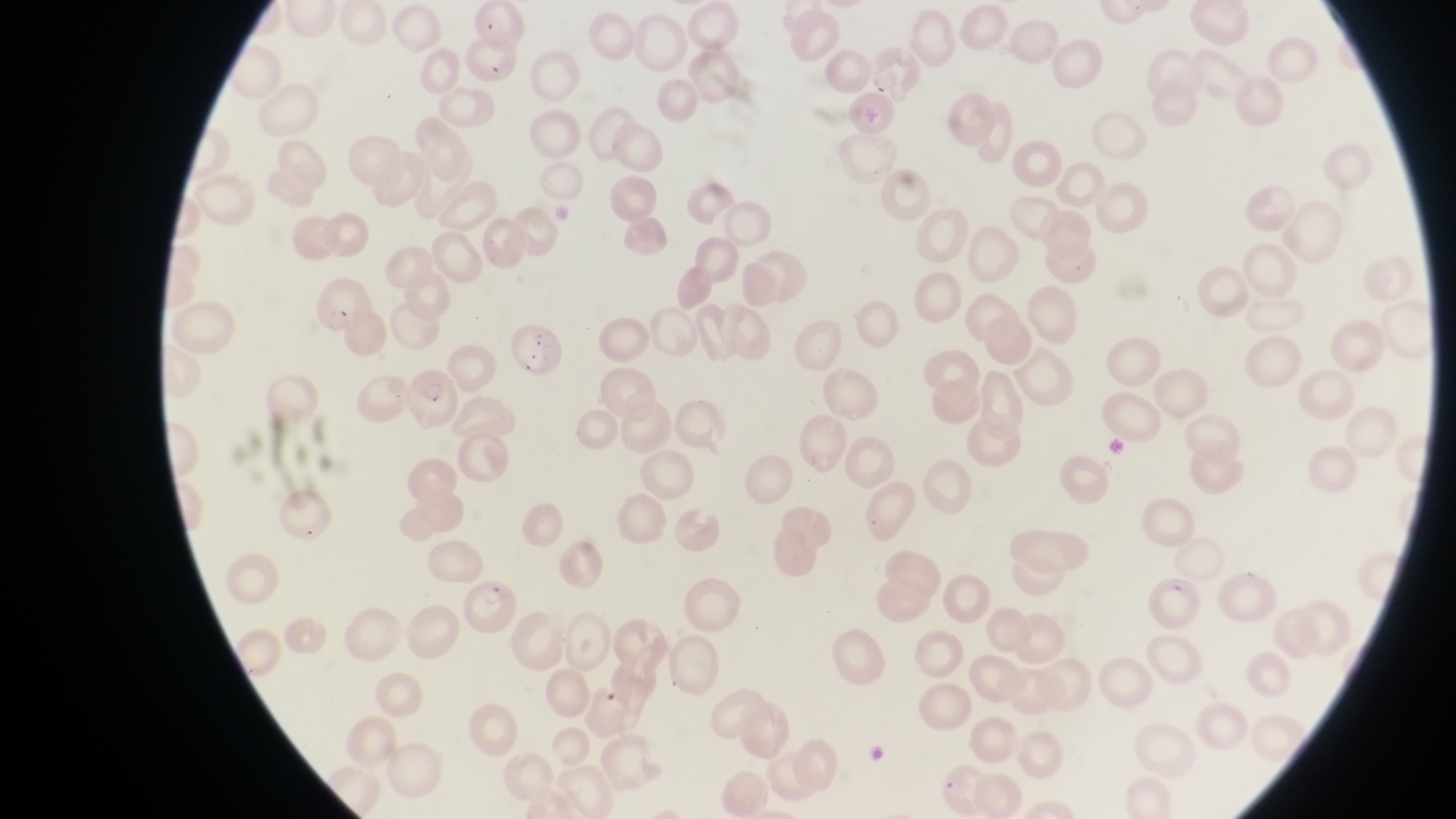
country = Uganda
image size = 1456×819 pixels
magnification = 1000x
parasitised red blood cell locations = approximate bounding boxes as (left, top, right, bottom) in pixels: (865, 45, 925, 104), (508, 319, 565, 385), (404, 376, 454, 429), (1153, 568, 1205, 632), (457, 579, 523, 639)
capture = smartphone photograph through the eyepiece of an Olympus CX-23 microscope
preparation = thin blood smear
field of view = single